Locate and identify every blood parasite.
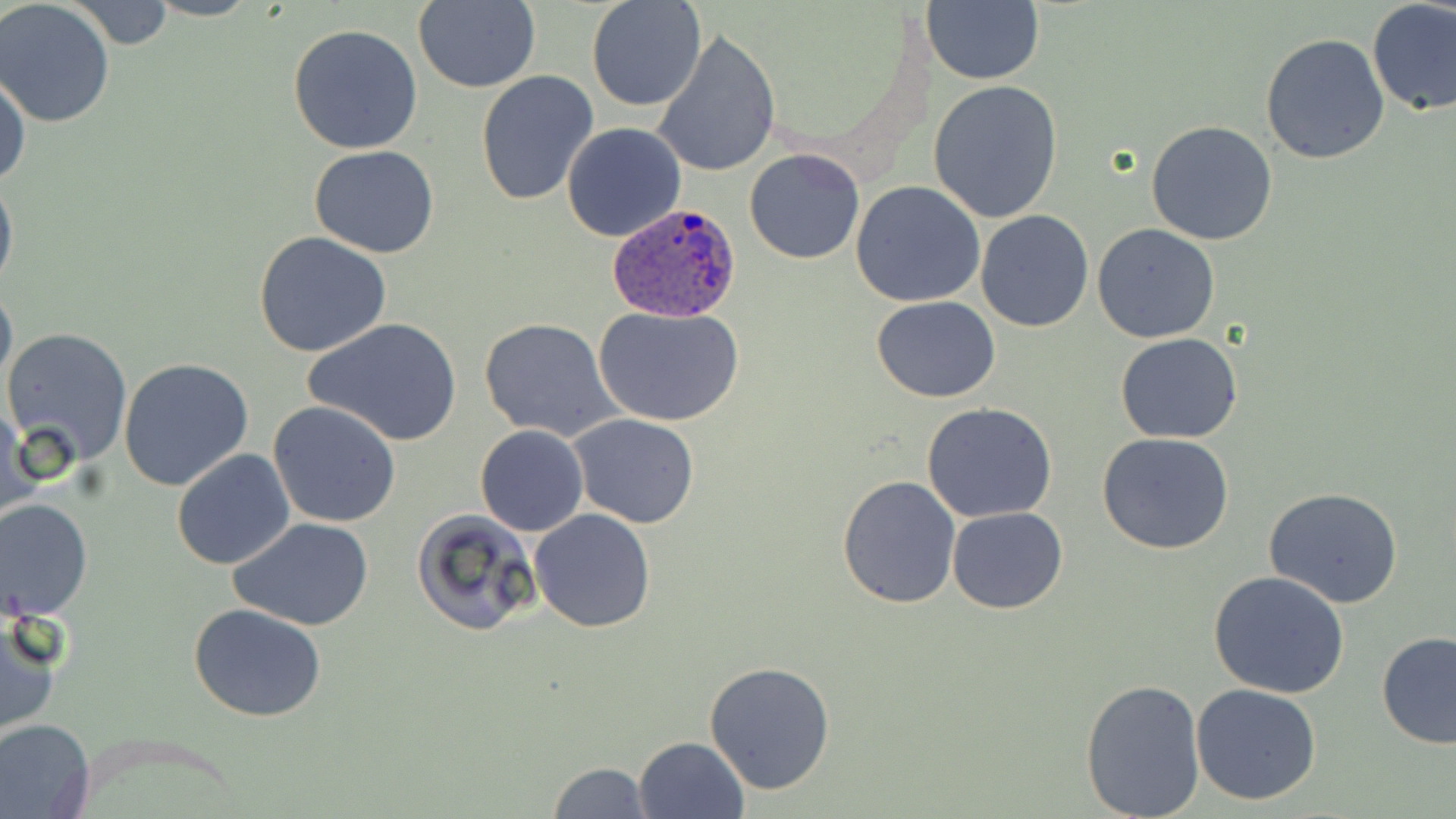
Approximate bounding boxes as [x1, y1, x2, y2] in pixels.
Plasmodium ovale-infected red blood cells: [608, 200, 742, 322].
No Plasmodium falciparum, Plasmodium malariae, Plasmodium vivax, Babesia divergens, or Trypanosoma brucei observed.

slide-level diagnosis = Plasmodium ovale
magnification = 1000x
image size = 1456×819 pixels
field of view = one of a larger specimen
stain = May-Grünwald-Giemsa
preparation = thin blood smear
modality = optical microscopy
uninfected red blood cell locations = approximate bounding boxes as [x1, y1, x2, y2] in pixels: [412, 0, 540, 93], [68, 1, 179, 51], [586, 1, 706, 112], [923, 1, 1043, 86], [1365, 1, 1455, 116], [0, 2, 117, 126], [287, 23, 423, 154], [652, 28, 780, 179], [1261, 32, 1390, 165], [1, 69, 30, 190], [475, 72, 600, 209], [928, 81, 1063, 224], [1146, 119, 1279, 245], [562, 121, 687, 243], [308, 146, 440, 258], [743, 147, 865, 265], [0, 166, 18, 301], [851, 181, 986, 306], [974, 209, 1093, 332], [1092, 224, 1220, 344], [253, 231, 392, 358], [0, 276, 16, 401], [871, 296, 1001, 403], [592, 305, 746, 426], [303, 317, 461, 448], [477, 317, 625, 444], [2, 327, 133, 468], [1116, 333, 1243, 443], [118, 357, 255, 492], [268, 401, 402, 530], [922, 402, 1058, 522], [1, 404, 39, 530], [569, 414, 700, 529], [475, 425, 589, 537], [1098, 434, 1237, 555], [171, 448, 295, 570], [836, 476, 963, 609], [1264, 489, 1405, 609], [0, 497, 94, 621], [529, 508, 656, 632], [948, 508, 1068, 614], [411, 509, 542, 638], [230, 518, 376, 633], [1207, 570, 1353, 699], [187, 603, 329, 722], [0, 610, 63, 740], [1374, 631, 1456, 750], [703, 662, 837, 796], [1080, 676, 1206, 817], [1191, 682, 1323, 805], [0, 718, 96, 818], [634, 736, 750, 819], [544, 760, 652, 818]